Identify the parasite.
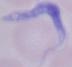

This is a trypanosome.

Photomicrograph. 1000x magnification.